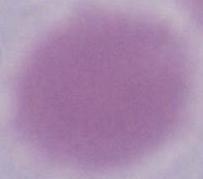
identification = erythrocyte
modality = photomicrograph
magnification = 1000x